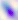

Summary:
  - Identification: Toxoplasma gondii
  - Magnification: 400x
  - Modality: micrograph